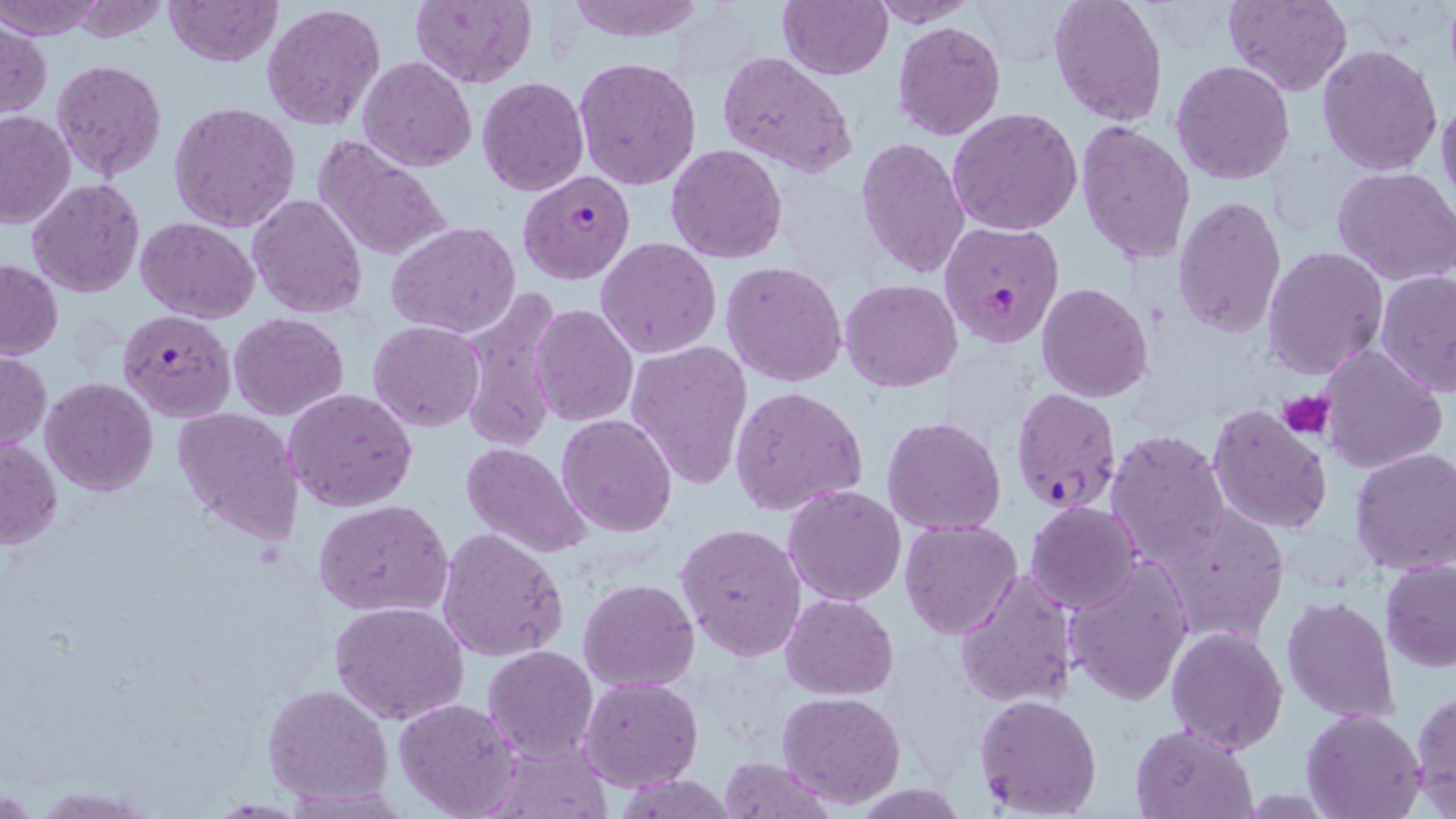 Approximate bounding boxes as (x1,y1)-(x2,y2) corner pairs in pixels. Plasmodium falciparum-infected red blood cell locations: (518,169)-(636,286), (940,221)-(1065,347), (118,307)-(236,423), (1010,387)-(1122,514). Uninfected red blood cell locations: (0,0)-(105,42), (65,0)-(174,44), (165,0)-(283,68), (410,0)-(539,89), (562,0)-(707,42), (776,0)-(892,79), (866,0)-(977,26), (1225,0)-(1351,98), (262,1)-(386,133), (1048,1)-(1168,127), (0,19)-(50,119), (891,20)-(1006,141), (1317,45)-(1442,176), (717,52)-(859,177), (573,55)-(704,191), (359,56)-(476,171), (51,60)-(169,183), (1171,60)-(1295,186), (476,76)-(589,197), (1437,90)-(1456,210), (169,100)-(301,232), (948,106)-(1082,236), (0,110)-(75,228), (1076,122)-(1198,267), (313,134)-(453,262), (856,136)-(972,279), (664,144)-(788,264), (1331,165)-(1456,284), (27,177)-(145,298), (248,192)-(366,318), (1173,196)-(1287,340), (136,217)-(258,323), (386,220)-(521,338), (596,236)-(722,358), (1261,245)-(1388,381), (0,259)-(62,360), (722,260)-(849,387), (1377,269)-(1456,399), (841,279)-(962,391), (1037,282)-(1154,401), (457,290)-(564,451), (531,303)-(638,428), (228,313)-(349,421), (369,321)-(486,431), (626,340)-(751,490), (1317,343)-(1448,472), (0,351)-(49,454), (41,377)-(159,496), (730,385)-(869,518), (284,388)-(417,513), (1207,401)-(1334,535), (173,406)-(304,548), (556,413)-(676,537), (881,417)-(1006,536), (1106,427)-(1231,565), (1,438)-(62,550), (463,442)-(594,559), (1349,447)-(1456,575), (783,485)-(906,607), (313,499)-(454,617), (1025,502)-(1144,614), (1154,505)-(1287,643), (899,519)-(1022,640), (675,522)-(807,662), (437,528)-(568,664), (1065,559)-(1194,707), (1379,559)-(1456,672), (953,570)-(1079,710), (579,577)-(701,692), (782,593)-(897,698), (1282,595)-(1400,724), (329,600)-(469,724), (1166,626)-(1288,753), (482,646)-(599,763), (580,676)-(703,791), (262,682)-(393,807), (1410,689)-(1455,811), (777,692)-(906,809), (973,693)-(1105,818), (392,697)-(522,818), (1303,709)-(1425,819), (1130,722)-(1259,818), (488,741)-(613,818), (716,755)-(833,818), (616,775)-(741,817), (29,785)-(164,818). Platelet locations: (1280,389)-(1334,441). Slide-level diagnosis: Plasmodium falciparum. Thin blood film. Image is 1456×819 pixels. 1000x magnification. One field of a larger specimen. May-Grünwald-Giemsa-stained preparation. Optical microscopy.